Locate every Plasmodium malariae-infected red blood cell.
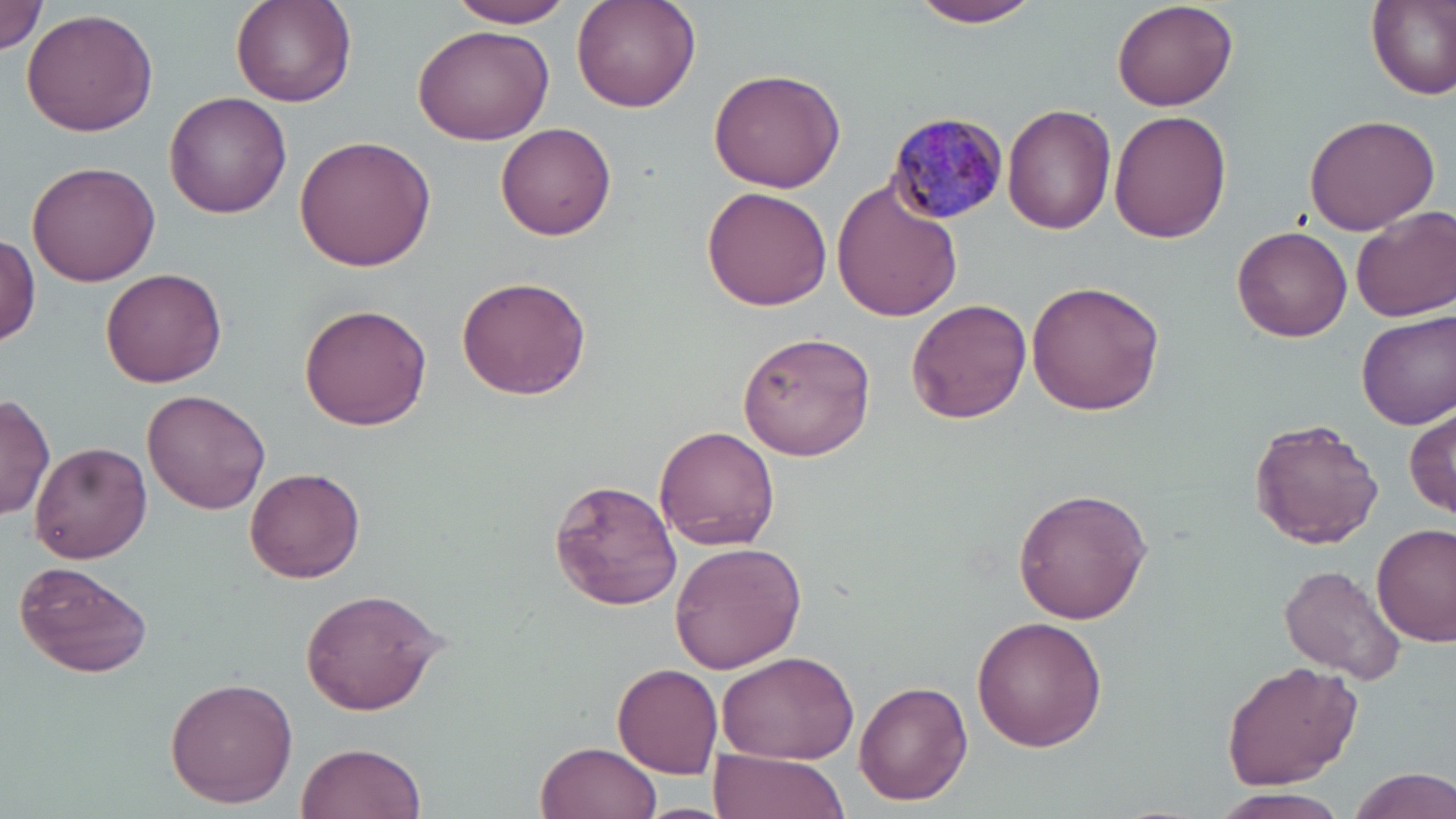

Approximate bounding boxes as (x1, y1, x2, y2) in pixels.
Plasmodium malariae-infected red blood cells: (887, 111, 1010, 225).

Uninfected red blood cell locations: (0, 0, 50, 58), (230, 0, 357, 109), (444, 0, 577, 27), (570, 0, 703, 113), (908, 0, 1045, 27), (1365, 0, 1456, 101), (1111, 1, 1237, 110), (21, 7, 159, 138), (411, 22, 553, 147), (707, 65, 845, 192), (163, 91, 292, 219), (1004, 102, 1116, 234), (1109, 110, 1233, 245), (1302, 113, 1442, 236), (496, 122, 618, 240), (292, 134, 437, 272), (26, 160, 161, 286), (831, 179, 963, 322), (702, 188, 832, 312), (1352, 206, 1456, 322), (1232, 225, 1352, 343), (1, 233, 40, 343), (102, 268, 228, 390), (457, 276, 591, 400), (1026, 279, 1167, 416), (906, 299, 1031, 424), (300, 304, 434, 431), (1359, 311, 1456, 429), (737, 330, 878, 462), (142, 389, 272, 515), (0, 394, 54, 521), (1406, 403, 1456, 520), (1248, 419, 1383, 549), (654, 425, 781, 551), (30, 442, 152, 564), (244, 466, 365, 584), (549, 477, 683, 611), (1011, 487, 1154, 623), (1373, 523, 1455, 647), (669, 540, 807, 673), (13, 559, 153, 679), (1279, 564, 1408, 685), (300, 586, 447, 717), (972, 616, 1108, 753), (716, 647, 859, 766), (1221, 660, 1361, 792), (612, 663, 722, 779), (164, 676, 298, 809), (853, 679, 972, 806), (535, 740, 662, 819), (295, 742, 427, 819), (709, 749, 848, 819), (1342, 765, 1456, 819), (1207, 789, 1354, 819), (631, 802, 740, 819). Slide-level diagnosis: Plasmodium malariae. Captured at 1000x magnification. Thin blood smear. May-Grünwald-Giemsa-stained preparation. Single field of view. Image is 1456×819 pixels. Light microscopy.